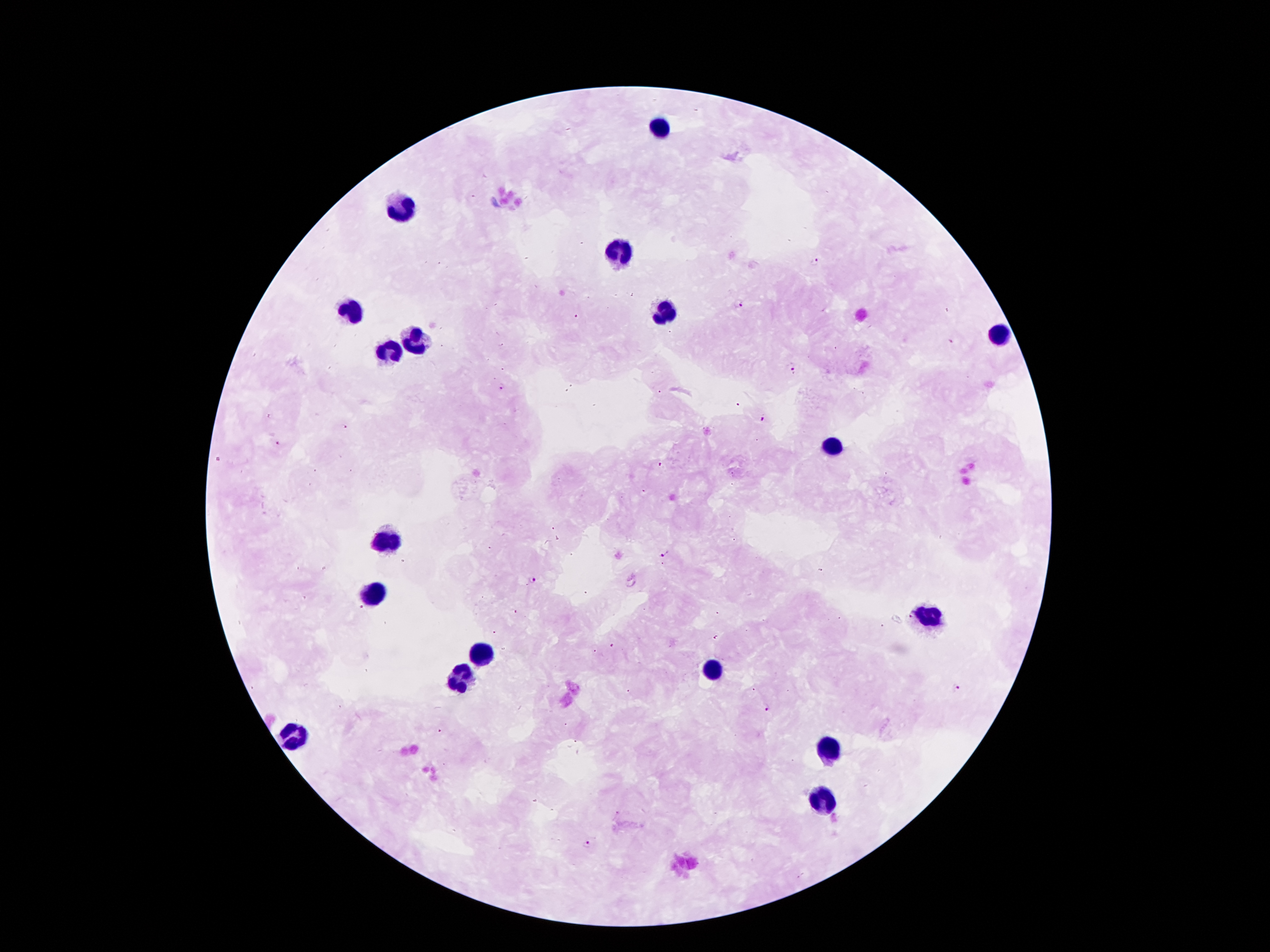

Approximate object centers, in pixels from the top-left corner.
Summary:
  - Plasmodium parasite locations: (x=814, y=261), (x=739, y=304), (x=952, y=342), (x=792, y=370), (x=501, y=387), (x=760, y=417), (x=278, y=443), (x=666, y=556), (x=532, y=580), (x=957, y=688), (x=768, y=706), (x=586, y=844)
  - Leukocyte locations: (x=662, y=129), (x=401, y=210), (x=623, y=253), (x=663, y=312), (x=353, y=313), (x=999, y=334), (x=413, y=341), (x=391, y=355), (x=833, y=447), (x=384, y=539), (x=376, y=595), (x=930, y=616), (x=481, y=656), (x=713, y=670), (x=460, y=679), (x=293, y=735), (x=830, y=747), (x=821, y=799)
  - Preparation: thick blood film
  - Capture: smartphone through the microscope eyepiece
  - Image size: 1270×952 pixels
  - Field of view: one from this slide
  - Patient malaria status: positive for Plasmodium falciparum
  - Magnification: 100x
  - Stain: Giemsa